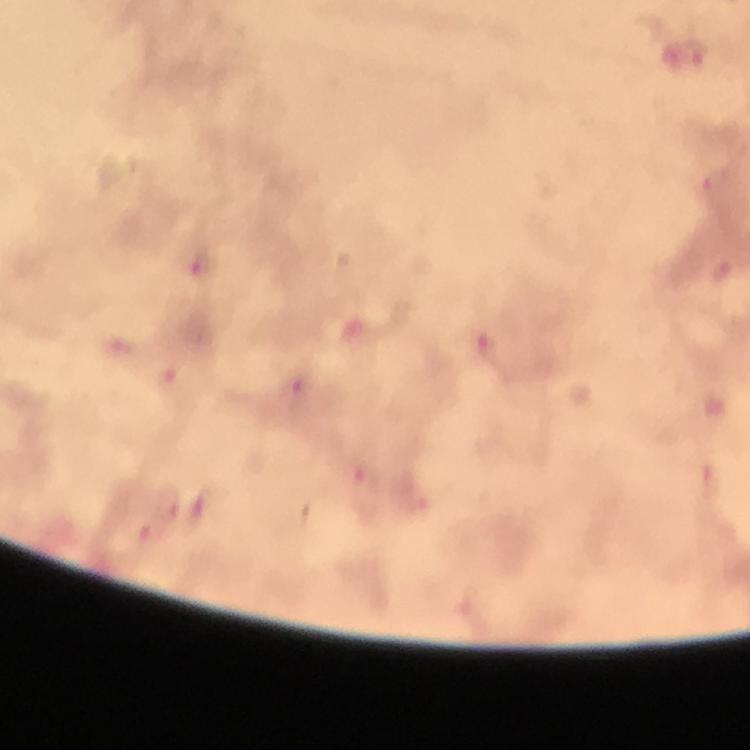
Approximate centers as {x, y} in pixels. Plasmodium parasite locations: {693, 54}, {716, 183}, {202, 265}, {491, 347}, {300, 385}, {367, 494}, {167, 503}. Photographed through the microscope with a smartphone camera. A crop from one field of view. Thick blood film. From a diagnostic examination for malaria. Immersion oil applied. Image is 750×750 pixels. At 100x magnification. Giemsa stain.